Look for Plasmodium parasites.
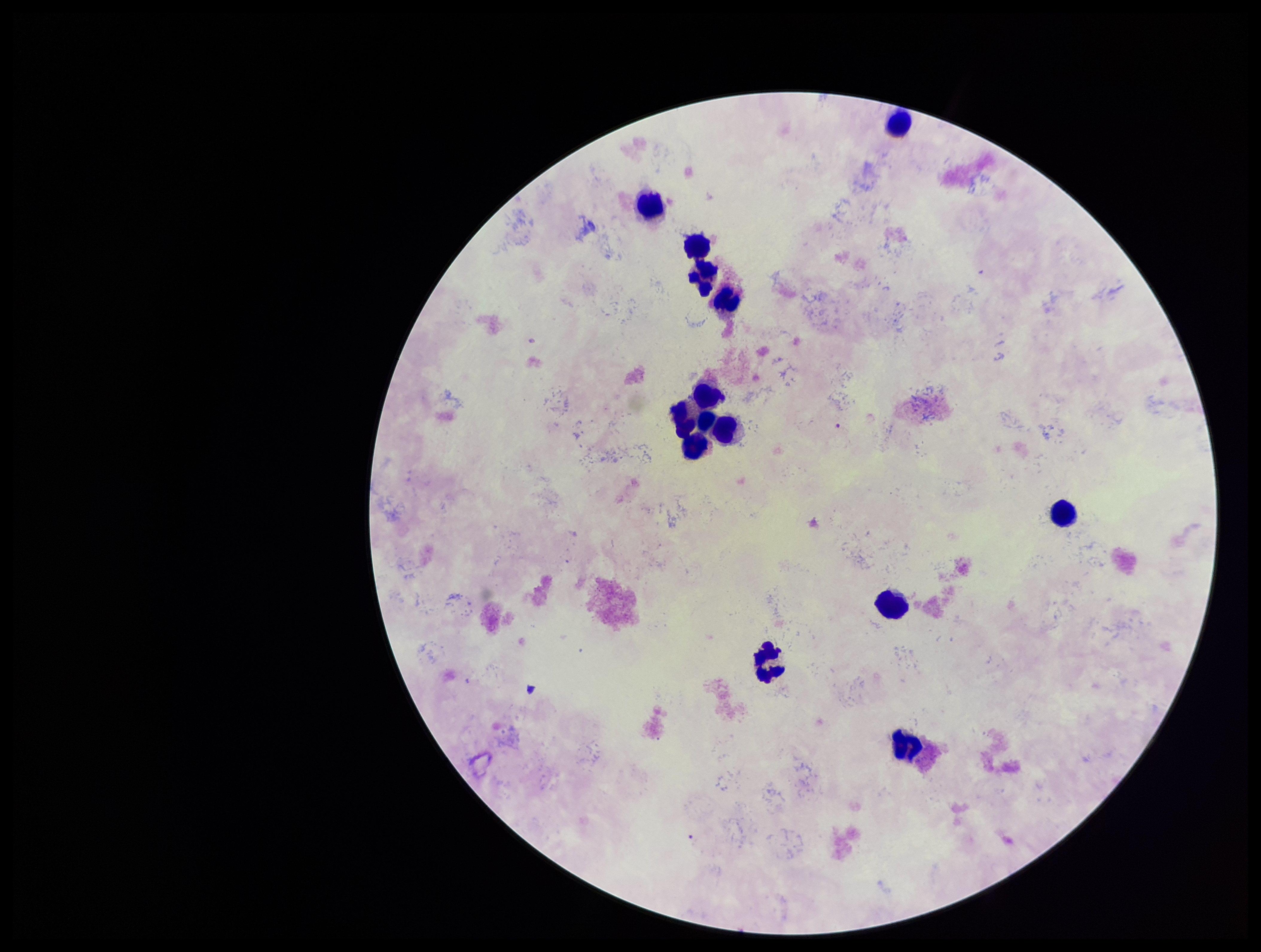
None seen.

Summary:
  - Species reported for this patient: Plasmodium falciparum
  - Image size: 1261×952 pixels
  - Leukocyte count: 14
  - Parasite count: 0
  - Field of view: single
  - Stain: Giemsa
  - Preparation: thick blood smear
  - Capture: smartphone photograph through the microscope eyepiece
  - Patient malaria status: infected